State which parasite is depicted.
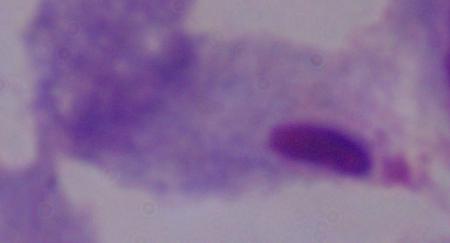
A trichomonad.

Photomicrograph. 1000x magnification.